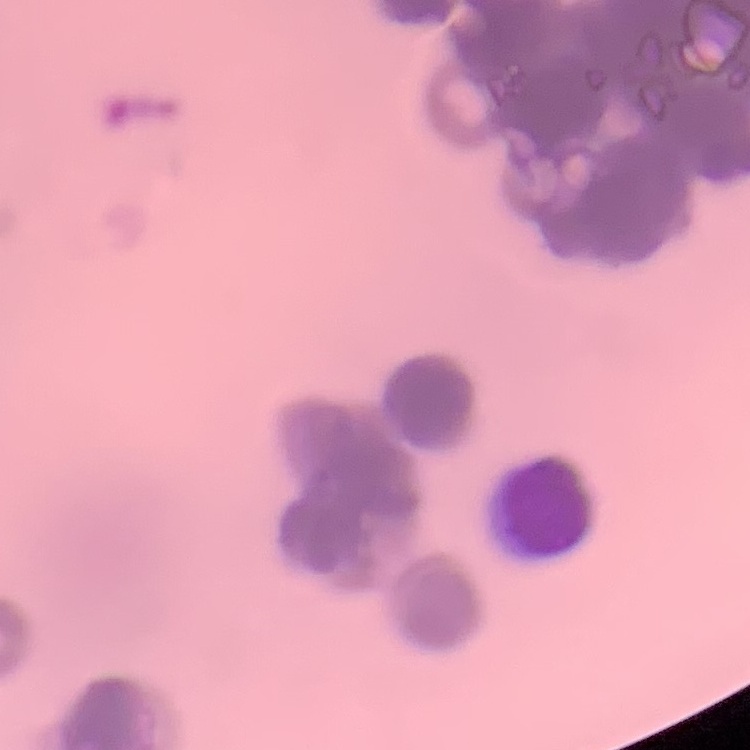
The red blood cells exhibit rouleaux formation. Thin blood smear. Square crop of a larger photomicrograph. Stained with either Field's or Giemsa.